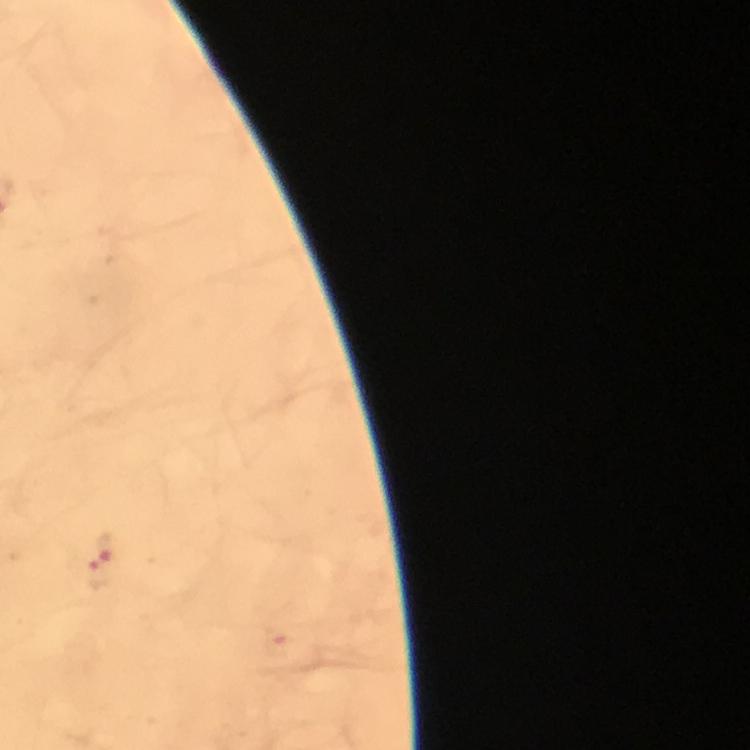

Approximate centers as (x, y) in pixels. Malaria parasite locations: (108, 545), (100, 573), (278, 642). Smartphone photograph taken through a microscope. From a malaria diagnostic workup. Giemsa stain. Thick smear. Cropped region of a single field of view. At 100x magnification. Immersion oil was used. Image is 750×750 pixels.